Assess this cell for malaria.
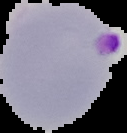
Parasitized.

Summary:
  - Image size: 127×133 pixels
  - Preparation: thin blood smear
  - Image type: segmented cell region on a black background